Locate every leukocyte (white blood cell).
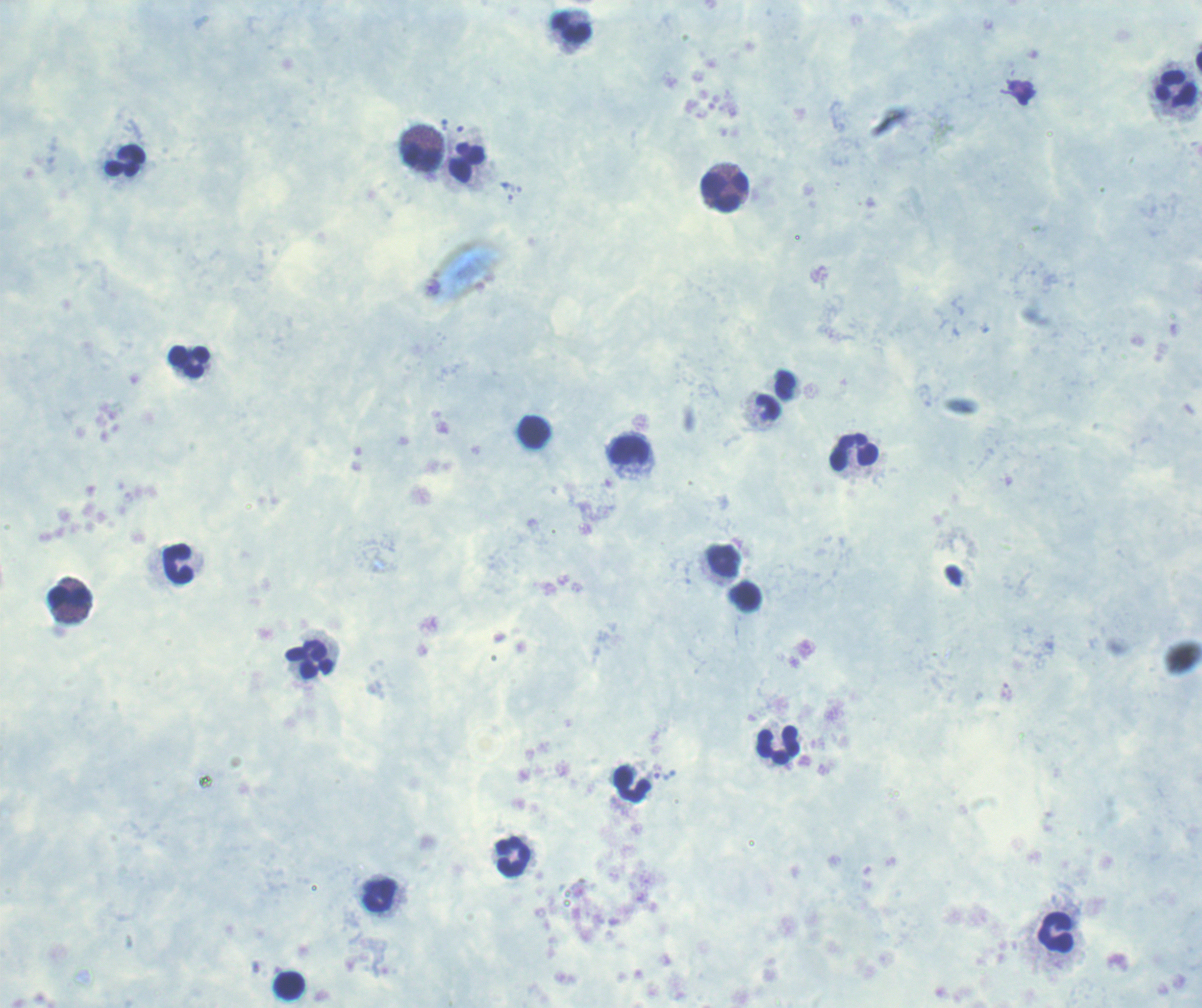
Approximate centers as [x, y] in pixels.
Leukocytes: [572, 29], [1176, 89], [423, 158], [127, 161], [465, 164], [725, 192], [188, 362], [769, 409], [535, 432], [630, 450], [854, 453], [722, 561], [178, 565], [748, 597], [72, 598], [309, 660], [778, 746], [633, 784], [513, 858], [379, 897], [1055, 932], [289, 986].

Summary:
  - Result: no Plasmodium parasites seen
  - Context: previously used in a real diagnosis
  - Field of view: single
  - Preparation: thick blood film
  - Image size: 1202×1008 pixels
  - Background quality: unsatisfactory
  - Stain: Romanowsky
  - Magnification: 100x